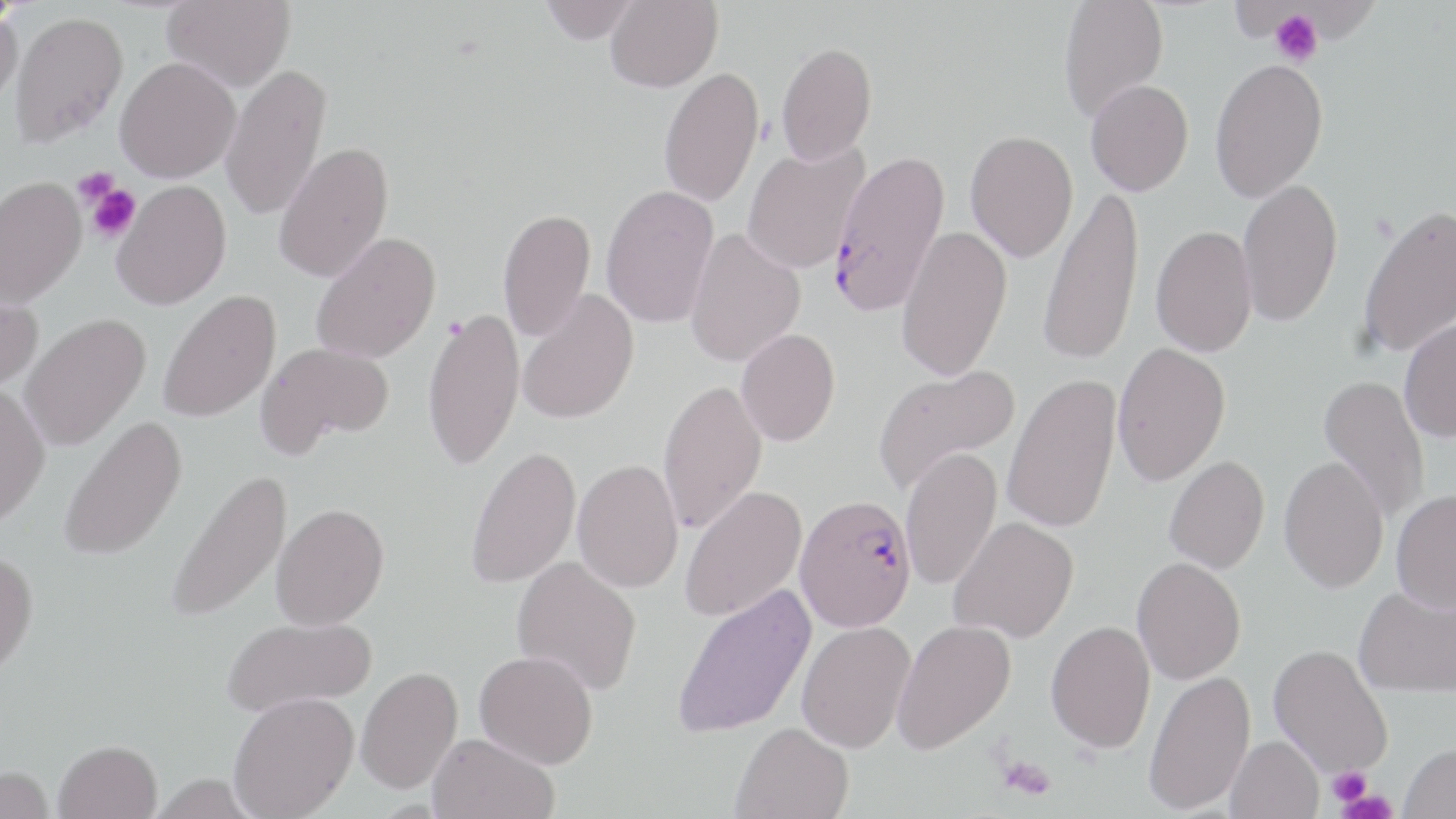

Approximate bounding boxes as [x1, y1, x2, y2] in pixels. Plasmodium falciparum-infected red blood cell locations: [827, 149, 950, 317], [794, 493, 918, 632]. Uninfected red blood cell locations: [0, 0, 26, 29], [162, 0, 296, 91], [539, 0, 640, 43], [606, 0, 722, 92], [1058, 0, 1169, 123], [0, 9, 23, 113], [8, 10, 129, 148], [776, 41, 877, 165], [115, 56, 240, 182], [1209, 57, 1328, 203], [220, 64, 331, 221], [658, 66, 764, 207], [1085, 79, 1194, 195], [965, 130, 1079, 261], [274, 141, 394, 283], [741, 142, 869, 274], [0, 176, 87, 309], [1237, 179, 1343, 327], [111, 180, 231, 310], [1037, 183, 1146, 367], [601, 184, 720, 329], [1357, 202, 1456, 358], [497, 207, 595, 342], [896, 225, 1013, 381], [1151, 225, 1257, 357], [685, 228, 806, 367], [311, 232, 441, 364], [517, 288, 639, 425], [0, 289, 42, 393], [159, 289, 281, 422], [423, 308, 525, 472], [20, 313, 151, 451], [1399, 316, 1456, 442], [736, 328, 840, 446], [1112, 341, 1231, 486], [257, 342, 393, 458], [872, 364, 1019, 494], [1002, 373, 1122, 534], [1318, 375, 1430, 524], [658, 379, 767, 534], [0, 384, 51, 529], [58, 415, 188, 563], [465, 445, 581, 589], [900, 447, 1003, 590], [1164, 456, 1270, 573], [1279, 456, 1389, 593], [572, 458, 684, 593], [166, 469, 293, 625], [679, 486, 807, 623], [1391, 489, 1456, 612], [272, 503, 389, 630], [949, 516, 1079, 643], [0, 549, 39, 680], [1132, 556, 1246, 685], [512, 557, 642, 696], [671, 583, 816, 740], [1354, 584, 1456, 698], [223, 616, 377, 717], [891, 620, 1016, 754], [1046, 620, 1155, 753], [796, 621, 915, 753], [1269, 644, 1393, 777], [474, 649, 598, 767], [356, 666, 463, 794], [1144, 670, 1255, 814], [228, 691, 360, 819], [732, 721, 854, 819], [427, 732, 560, 819], [1226, 735, 1324, 819], [54, 739, 162, 819], [1399, 742, 1456, 818], [0, 766, 55, 819]. Platelet locations: [1270, 9, 1323, 67], [73, 167, 120, 208], [83, 182, 140, 244], [997, 755, 1057, 799], [1327, 765, 1372, 807], [1333, 792, 1399, 819]. Slide-level diagnosis: Plasmodium falciparum. 1000x magnification. May-Grünwald-Giemsa-stained preparation. Single field of view. Light microscopy. Thin blood film. Image is 1456×819 pixels.